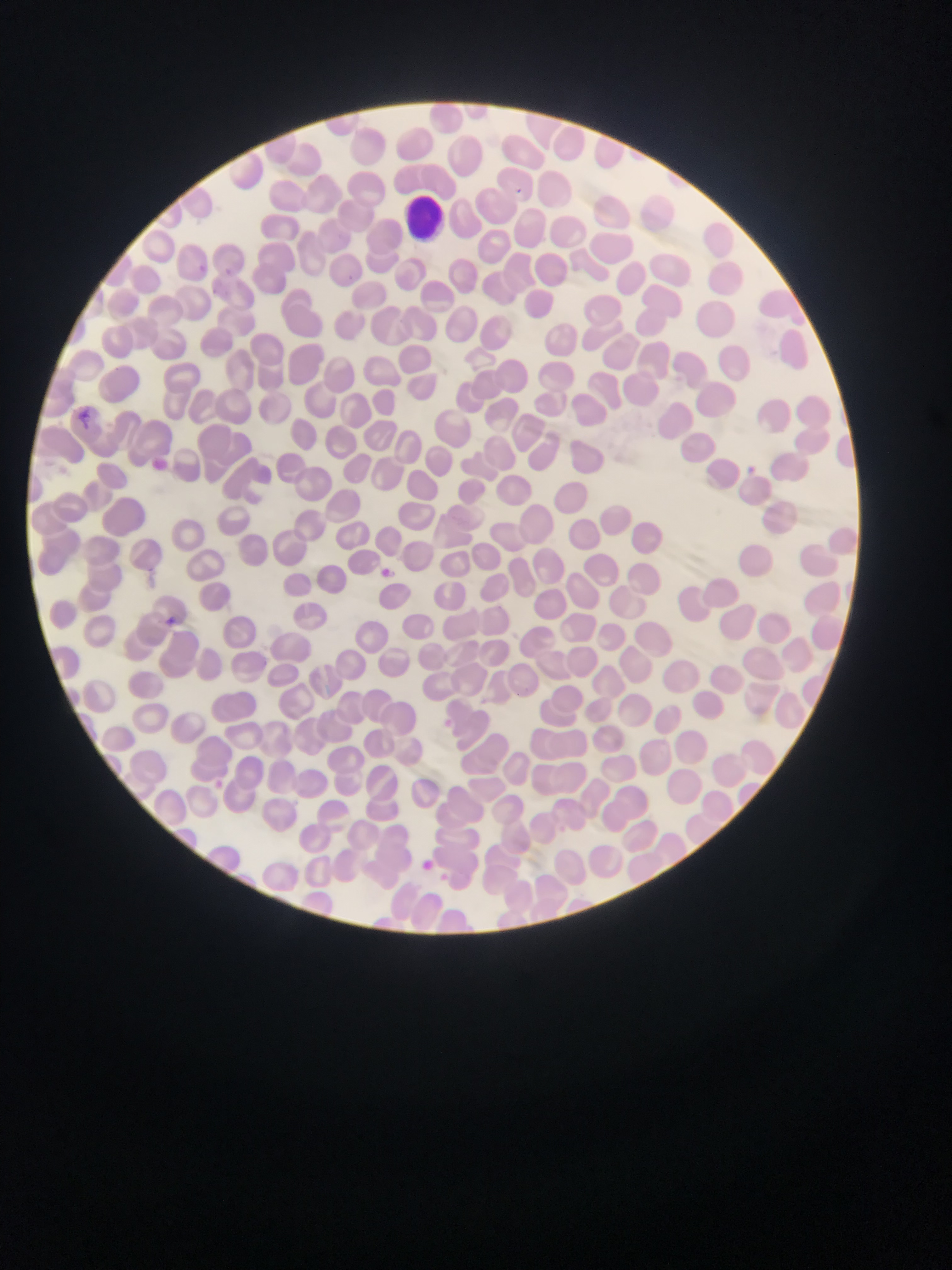
Approximate bounding boxes as [left, top, right, bottom] in pixels.
Summary:
  - Malaria parasite locations: [510, 184, 526, 199], [193, 260, 210, 277], [69, 407, 98, 432], [737, 462, 760, 481], [378, 563, 395, 580], [161, 614, 179, 630], [416, 856, 437, 875], [437, 870, 453, 884]
  - Leukocyte locations: [406, 198, 448, 239]
  - Preparation: thin blood smear
  - Image size: 952×1270 pixels
  - Country: Ghana
  - Capture: mobile-phone photograph through a microscope
  - Field of view: single